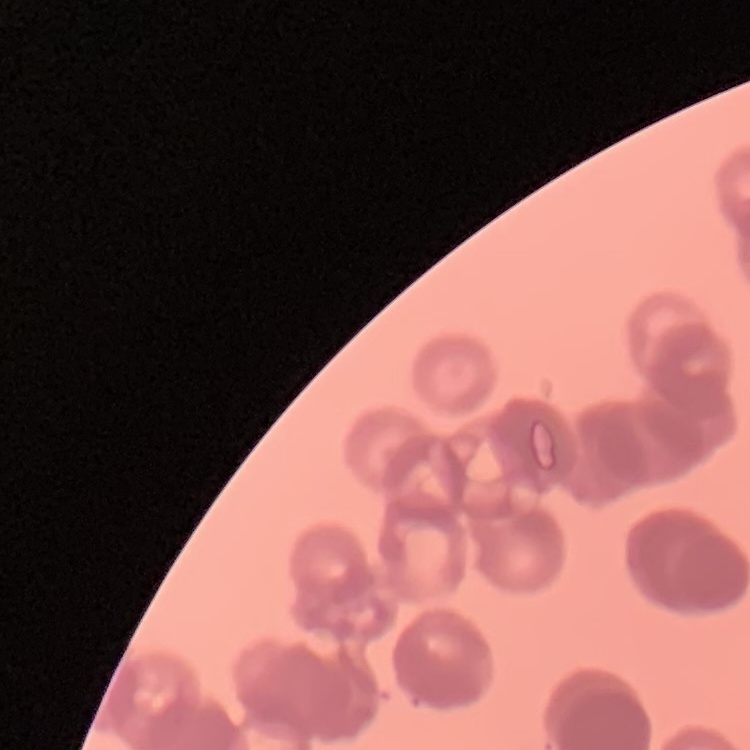

red blood cell morphology = rouleaux formation
image type = one tile cut from a larger photomicrograph
stain = Field's or Giemsa
preparation = thin blood film